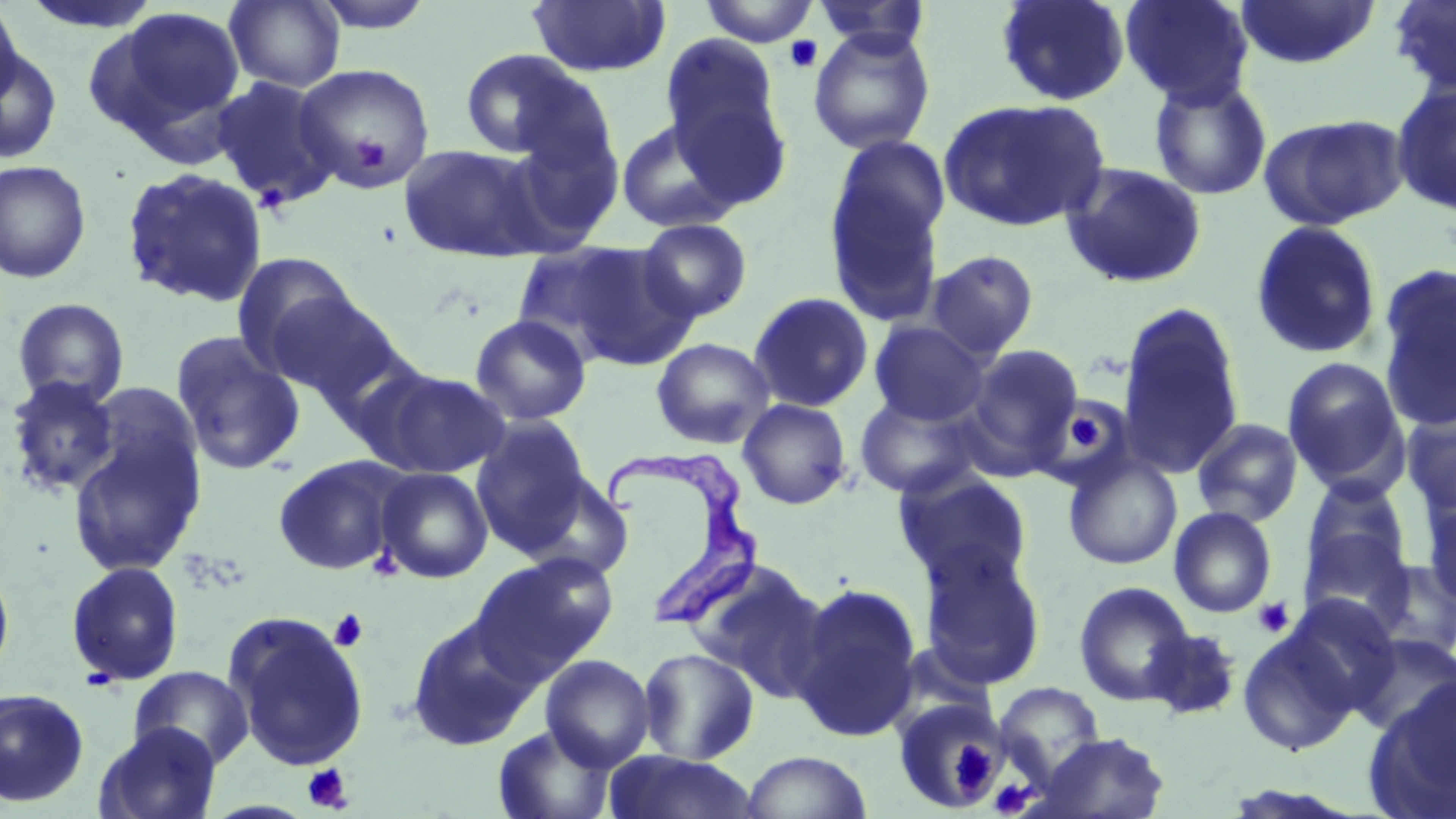
slide-level diagnosis = Trypanosoma brucei
preparation = thin blood film
modality = optical microscopy
field of view = one of a larger specimen
magnification = 1000x
stain = May-Grünwald-Giemsa
image size = 1456×819 pixels
Trypanosoma brucei locations = approximate bounding boxes as (x1,y1)-(x2,y2) corner pairs in pixels: (604,452)-(765,633)
uninfected red blood cell locations = approximate bounding boxes as (x1,y1)-(x2,y2) corner pairs in pixels: (0,0)-(24,112), (224,0)-(345,92), (308,0)-(439,34), (527,0)-(671,78), (699,0)-(819,46), (811,0)-(933,57), (994,0)-(1131,106), (1120,0)-(1256,107), (1234,0)-(1381,69), (1387,0)-(1456,97), (98,6)-(245,142), (807,27)-(936,155), (659,32)-(787,181), (0,46)-(62,164), (458,49)-(589,161), (293,62)-(436,191), (210,75)-(341,209), (1148,75)-(1273,201), (1390,81)-(1456,217), (938,98)-(1110,232), (1257,112)-(1409,230), (615,118)-(743,233), (398,144)-(546,263), (824,152)-(948,328), (0,159)-(92,283), (1060,161)-(1208,290), (120,166)-(269,309), (637,218)-(753,322), (1249,220)-(1384,360), (560,243)-(700,370), (510,244)-(649,361), (925,250)-(1040,360), (232,252)-(361,373), (1377,264)-(1456,430), (263,290)-(406,406), (748,291)-(874,413), (11,297)-(130,409), (1117,303)-(1246,479), (469,314)-(592,426), (868,320)-(990,426), (170,332)-(306,476), (651,337)-(775,450), (963,344)-(1085,468), (1281,357)-(1409,493), (364,368)-(511,478), (5,376)-(120,499), (86,382)-(203,493), (853,392)-(987,501), (737,398)-(853,510), (1402,403)-(1456,520), (471,416)-(592,553), (1191,417)-(1304,528), (67,425)-(206,577), (1062,452)-(1182,570), (272,455)-(408,575), (376,467)-(493,583), (893,469)-(1033,589), (518,471)-(635,582), (1301,478)-(1413,591), (1420,495)-(1456,611), (1169,507)-(1277,618), (1301,531)-(1415,630), (918,545)-(1047,689), (472,554)-(618,681), (1361,557)-(1456,661), (0,559)-(15,685), (65,560)-(185,687), (684,560)-(831,700), (1074,581)-(1195,706), (790,582)-(923,741), (225,615)-(368,770), (406,616)-(536,751), (1237,625)-(1362,757), (1142,627)-(1243,720), (1348,632)-(1456,740), (638,648)-(759,764), (540,654)-(656,772), (129,666)-(254,769), (1367,678)-(1456,818), (993,682)-(1107,785), (0,688)-(90,808), (893,699)-(1006,813), (95,722)-(221,819), (493,723)-(617,819), (1036,732)-(1170,819), (741,750)-(872,819), (604,751)-(761,819)
platelet locations = approximate bounding boxes as (x1,y1)-(x2,y2) corner pairs in pixels: (784,36)-(822,73), (352,132)-(391,171), (1055,401)-(1122,467), (1067,414)-(1104,451), (1253,597)-(1294,639), (329,608)-(369,653), (79,666)-(122,692), (953,738)-(1000,786), (302,763)-(353,813), (989,780)-(1032,816)